Assess for malaria.
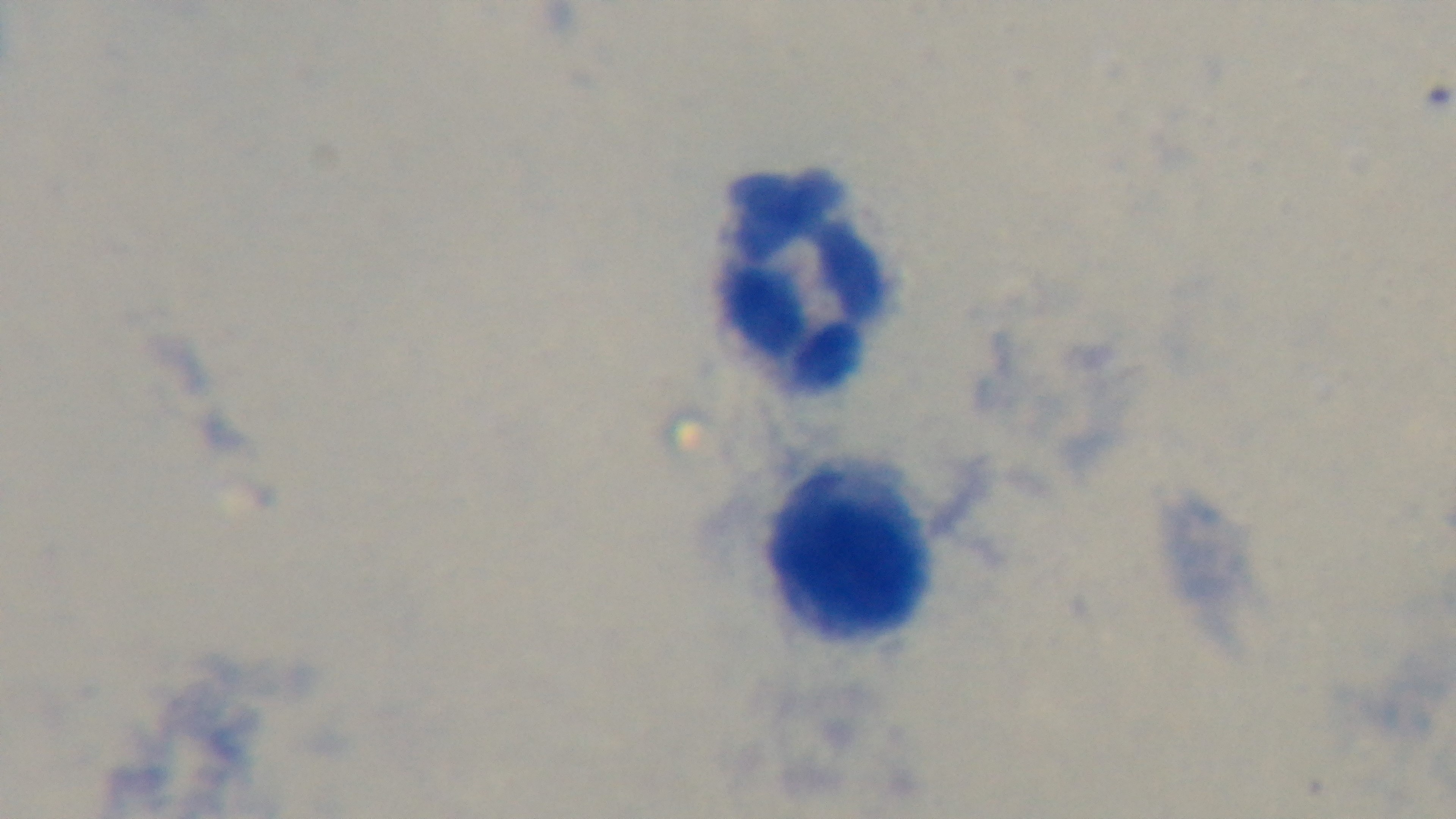
Negative.

{
  "modality": "light microscopy",
  "preparation": "thick",
  "stain": "Giemsa",
  "field_of_view": "single",
  "objective": "100x oil immersion",
  "capture": "mounted 4K digital camera"
}